Classify this cell by malaria status.
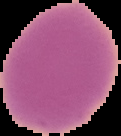

Uninfected.

Summary:
  - Image type: cell region segmented out of the field of view; surrounding area masked to black
  - Image size: 121×136 pixels
  - Preparation: thin blood film